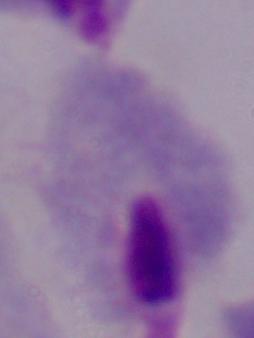 Micrograph. A trichomonad is seen. 1000x magnification.